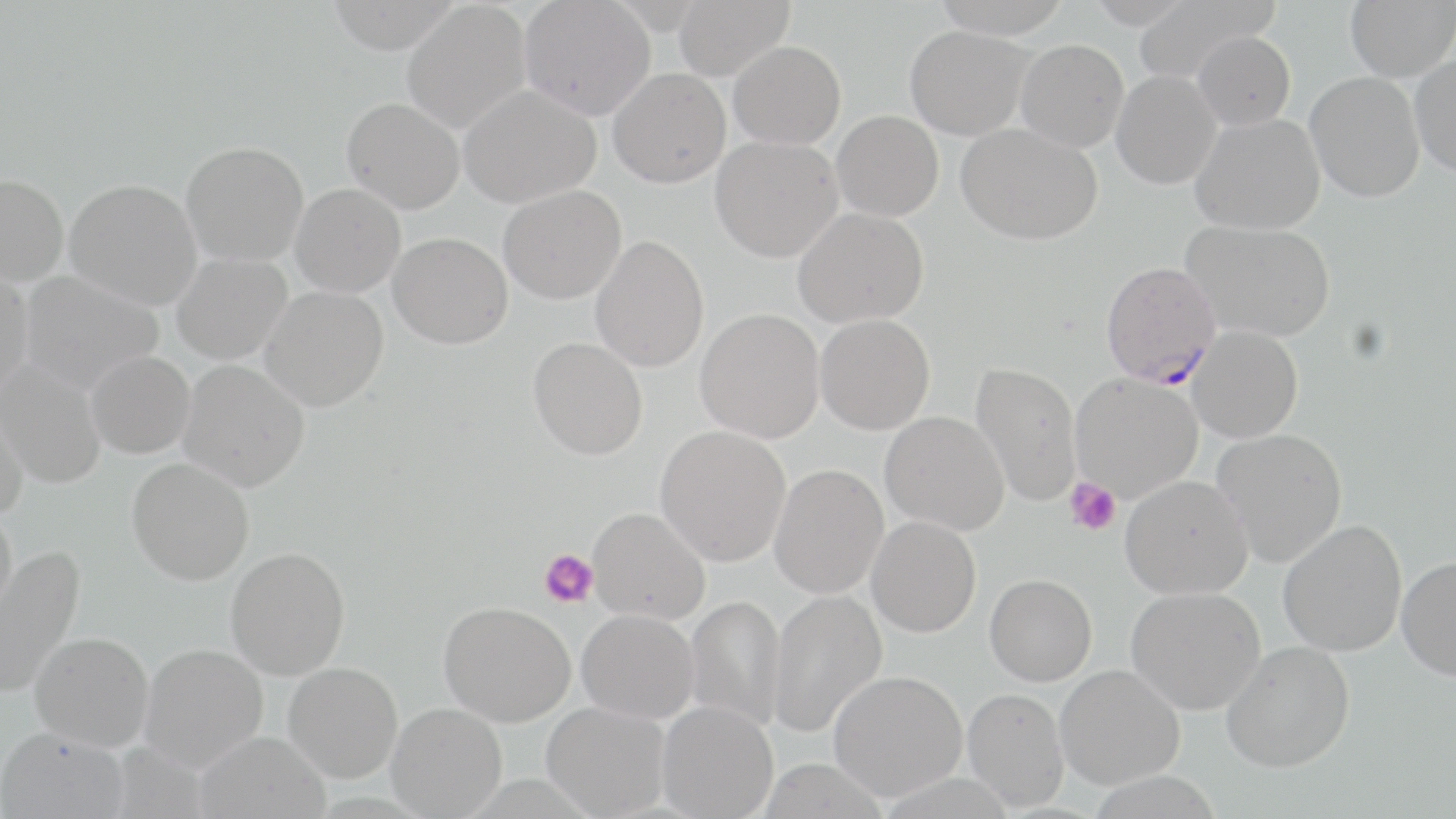
Approximate bounding boxes as [x1, y1, x2, y2] in pixels. Plasmodium falciparum-infected red blood cell locations: [1100, 260, 1222, 389]. Platelet locations: [1065, 478, 1121, 537], [540, 549, 598, 607]. Uninfected red blood cell locations: [326, 0, 462, 54], [519, 0, 656, 120], [672, 0, 794, 81], [930, 0, 1073, 39], [1082, 0, 1198, 27], [1135, 0, 1275, 82], [1345, 0, 1455, 81], [402, 3, 531, 134], [905, 25, 1033, 140], [1192, 31, 1296, 131], [1016, 39, 1129, 152], [728, 40, 846, 150], [1410, 54, 1456, 177], [608, 67, 731, 188], [1111, 70, 1222, 189], [1305, 71, 1425, 203], [459, 85, 601, 208], [341, 98, 465, 213], [832, 110, 944, 221], [1191, 113, 1325, 235], [956, 122, 1102, 245], [710, 135, 842, 262], [181, 141, 309, 266], [0, 174, 68, 286], [64, 178, 203, 311], [291, 183, 406, 297], [498, 185, 626, 304], [792, 207, 930, 328], [1181, 219, 1336, 342], [388, 232, 512, 349], [590, 235, 710, 373], [171, 252, 292, 365], [0, 266, 34, 402], [20, 270, 164, 395], [260, 285, 389, 411], [695, 308, 825, 443], [815, 314, 936, 434], [1187, 325, 1304, 443], [528, 337, 648, 460], [86, 350, 195, 458], [1, 358, 107, 490], [178, 359, 310, 491], [970, 361, 1081, 508], [1070, 373, 1203, 501], [0, 394, 29, 521], [880, 410, 1009, 536], [655, 424, 791, 567], [1211, 427, 1347, 566], [127, 457, 255, 585], [768, 464, 888, 599], [1120, 475, 1253, 599], [0, 506, 18, 625], [587, 507, 710, 624], [866, 516, 981, 637], [1277, 519, 1407, 656], [0, 544, 84, 698], [226, 546, 351, 680], [1396, 557, 1456, 680], [985, 574, 1097, 686], [1126, 587, 1266, 714], [767, 589, 887, 738], [685, 594, 786, 734], [438, 601, 576, 726], [577, 609, 699, 723], [30, 631, 154, 751], [1220, 641, 1355, 772], [140, 643, 268, 771], [283, 662, 403, 783], [1055, 664, 1185, 789], [828, 670, 967, 801], [962, 688, 1070, 811], [657, 701, 778, 819], [386, 702, 507, 818], [541, 702, 671, 817], [0, 726, 129, 819], [194, 730, 331, 819], [757, 758, 889, 818]. Slide-level diagnosis: Plasmodium falciparum. One field of a larger specimen. Thin blood film. Image is 1456×819 pixels. Captured at 1000x magnification. May-Grünwald-Giemsa-stained preparation. Light microscopy.